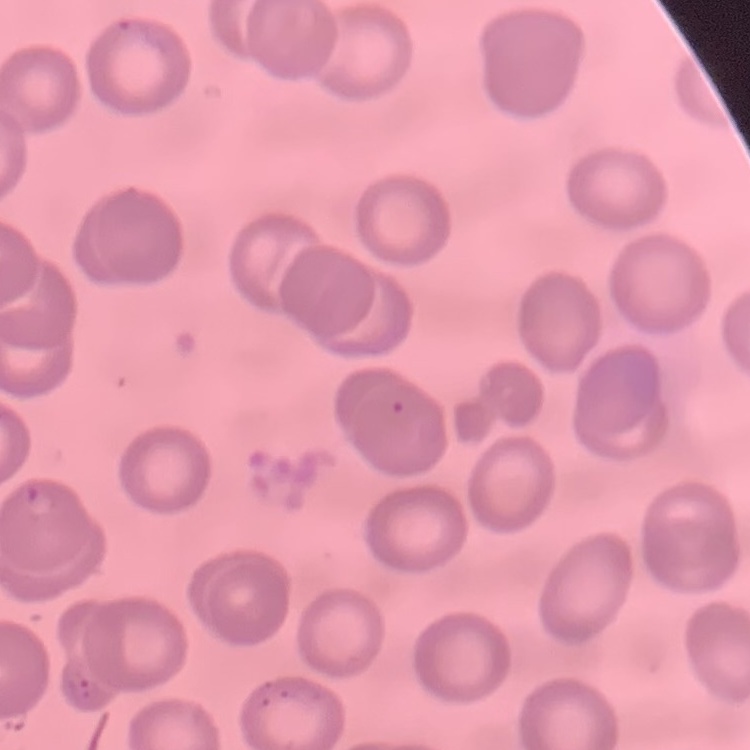
erythrocyte morphology = no rouleaux formation
preparation = thin peripheral smear
stain = Field's or Giemsa
image type = square crop of a larger photomicrograph